Report the malaria status.
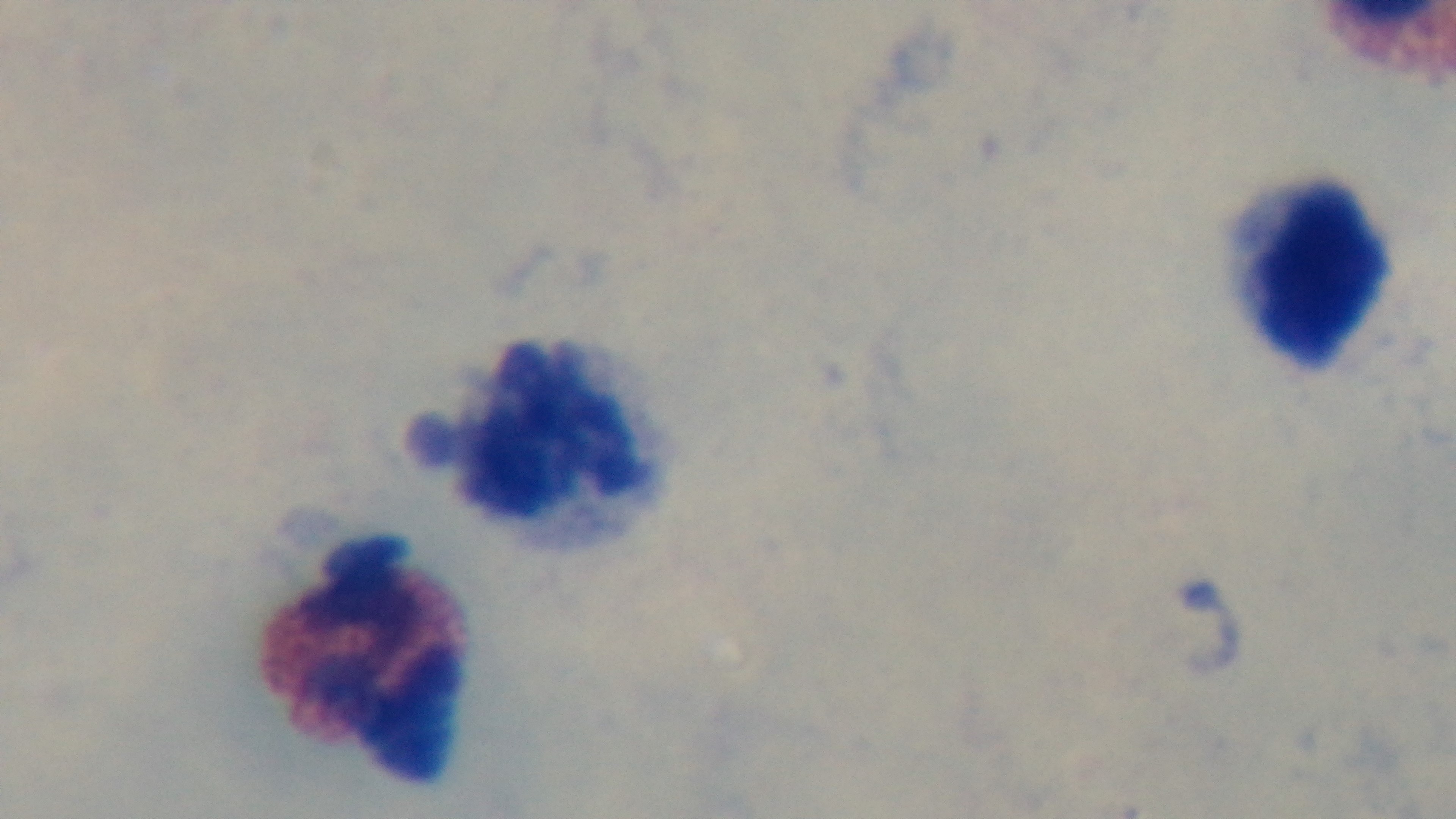

Negative.

Giemsa stain. Preparation: thick smear. Light microscopy. 100x oil-immersion objective. One field from the slide. Captured with a mounted 4K digital camera.